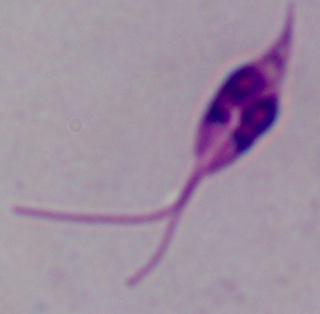

A Leishmania parasite is shown. Micrograph. 1000x magnification.